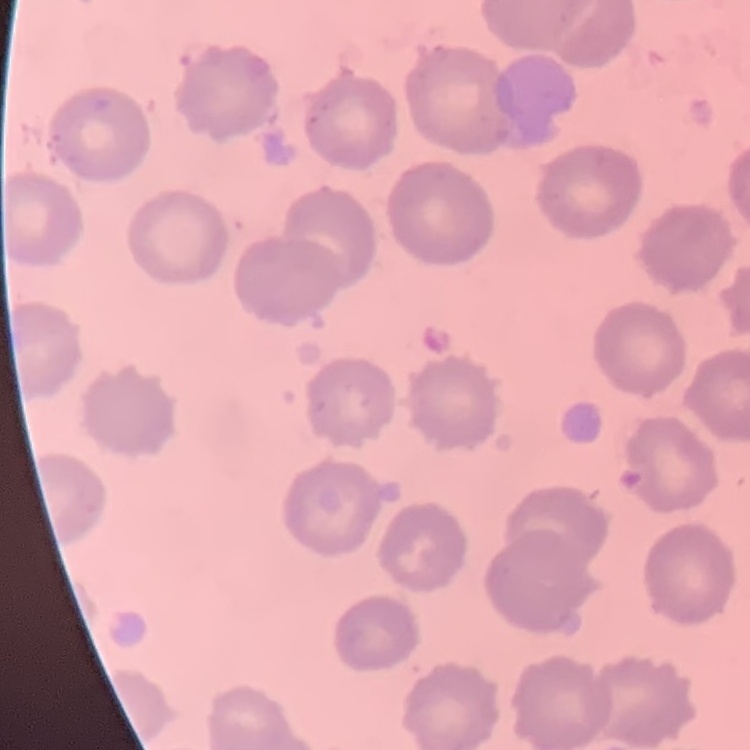

erythrocyte morphology = no rouleaux formation
image type = square crop of a larger photomicrograph
stain = Field's or Giemsa
preparation = thin blood film